Classify this cell by malaria status.
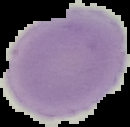

It is uninfected.

{
  "image_size": "130×127 pixels",
  "preparation": "thin blood smear",
  "image_type": "segmented cell region with the area outside set to black"
}